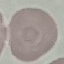

Summary:
  - Malaria status: uninfected
  - Stain: Giemsa
  - Preparation: thin blood film
  - Capture: smartphone through the microscope eyepiece
  - Image type: cell patch, automatically extracted from a larger field of view and resized to 64 × 64 pixels